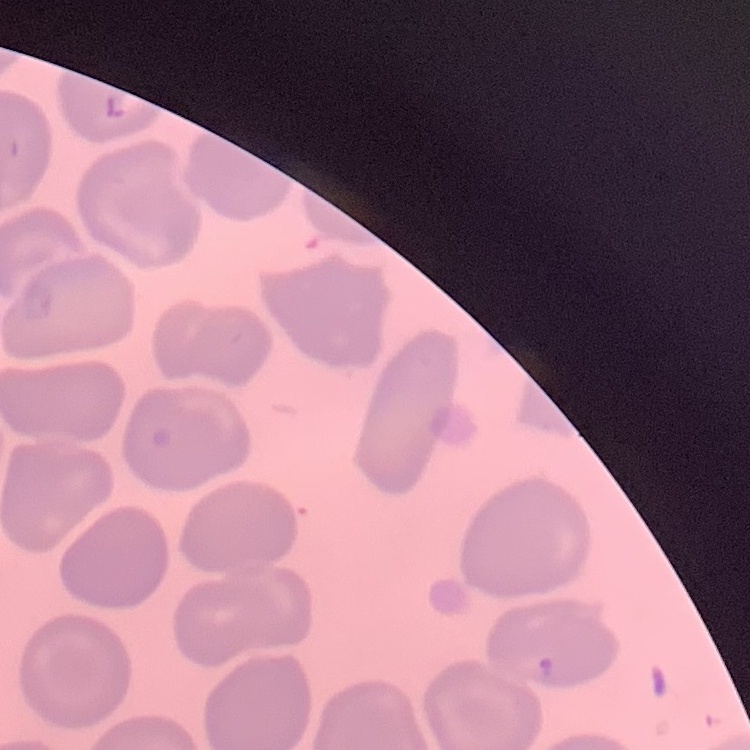
Summary:
  - Red blood cell morphology: no rouleaux formation
  - Stain: Field's or Giemsa
  - Preparation: thin blood smear
  - Image type: square crop of a larger photomicrograph